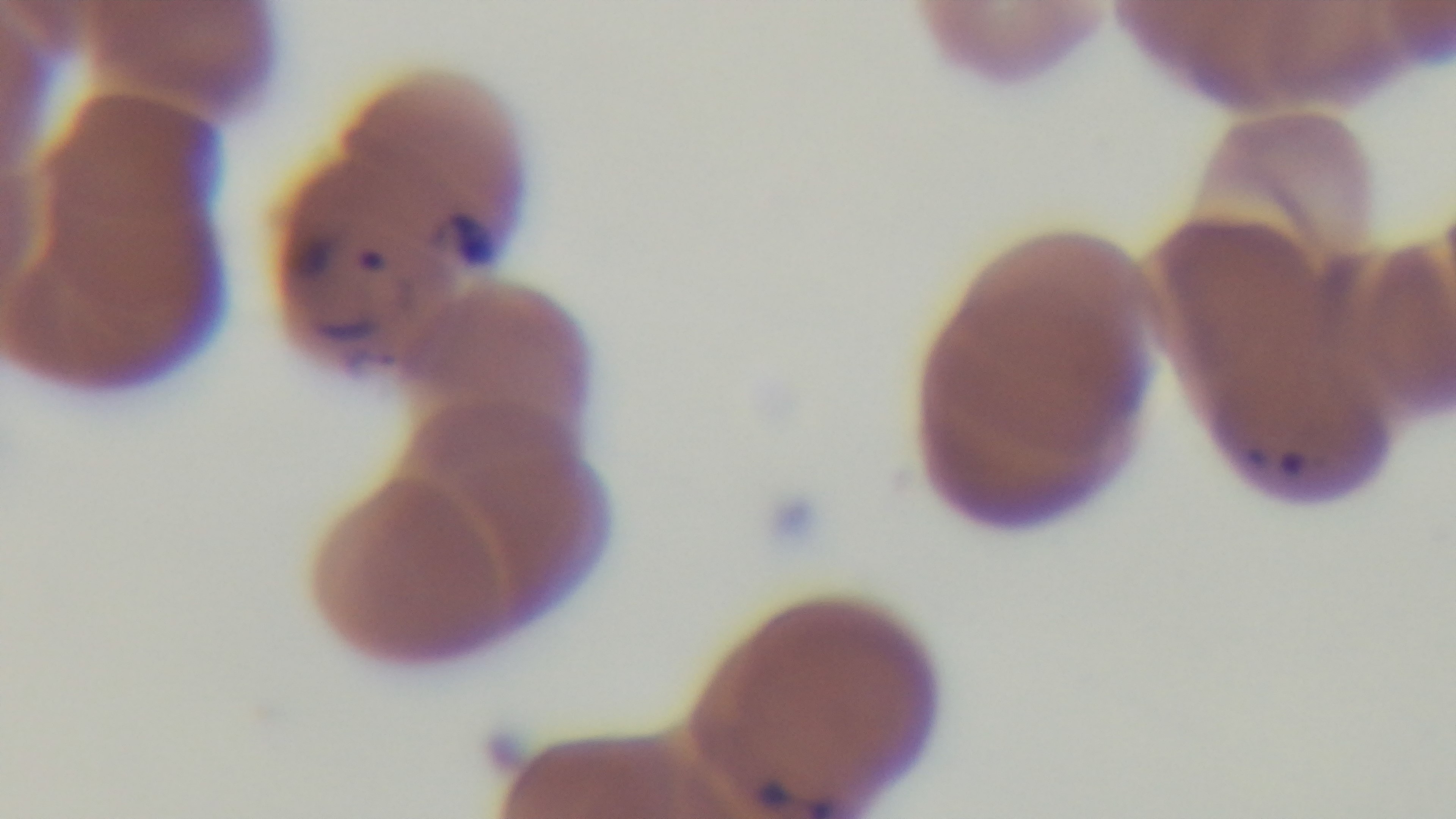
preparation = thin
modality = light microscopy
objective = 100x oil immersion
capture = mounted 4K digital camera
malaria status = positive
field of view = single
stain = Giemsa